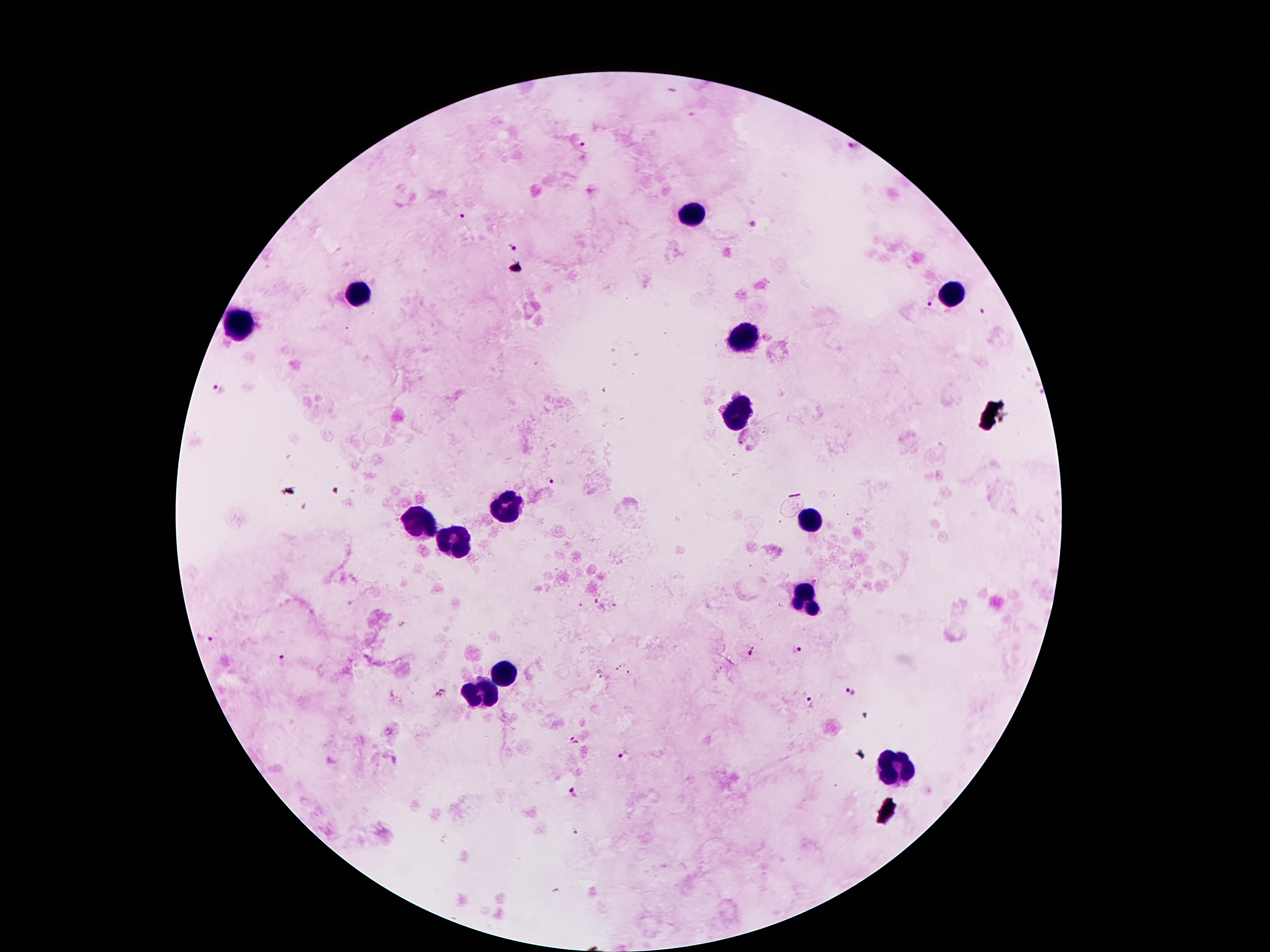

coordinate format = approximate centers as [x, y] in pixels
leukocyte locations = [695, 216], [361, 293], [953, 297], [239, 331], [743, 337], [737, 416], [512, 507], [809, 523], [422, 526], [454, 541], [806, 593], [502, 678], [481, 697], [897, 770]
Plasmodium parasite locations = [581, 145], [854, 147], [464, 216], [753, 225], [511, 247], [929, 302], [983, 312], [219, 390], [554, 482], [597, 606], [203, 638], [797, 650], [283, 662], [849, 692], [810, 702], [574, 741], [623, 754], [575, 795]
image size = 1270×952 pixels
preparation = thick blood film
field of view = single
patient malaria status = infected with Plasmodium falciparum
magnification = 100x
capture = smartphone through the microscope eyepiece
stain = Giemsa